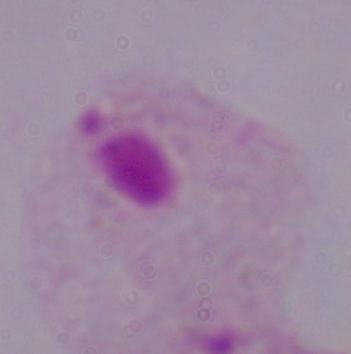
Summary:
  - Identification: trichomonad
  - Modality: photomicrograph
  - Magnification: 1000x